Report the malaria status of this cell.
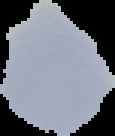
Uninfected.

preparation = thin blood smear
image size = 115×136 pixels
image type = segmented cell region with the area outside set to black